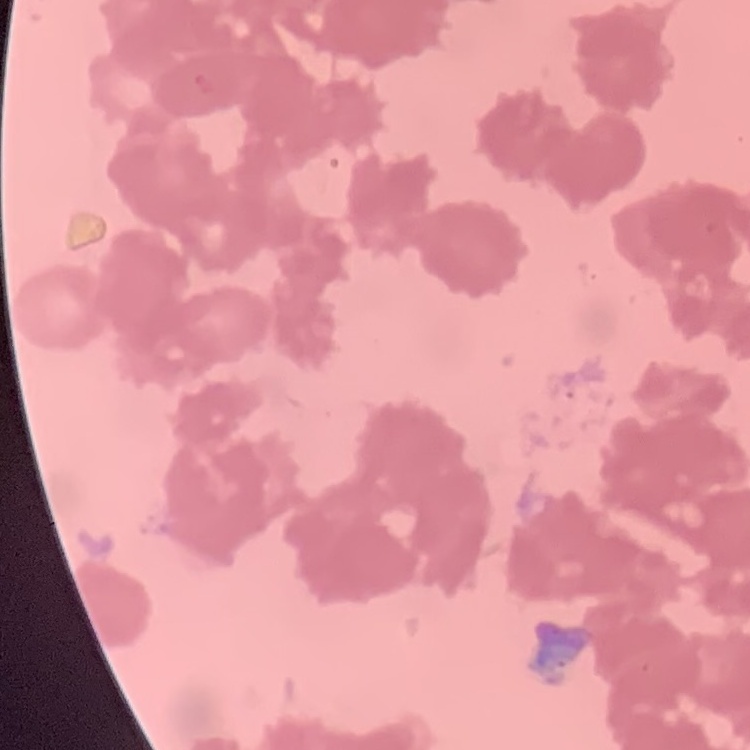

The erythrocytes exhibit rouleaux formation. Thin blood smear. Square crop of a larger photomicrograph. Stained with either Field's or Giemsa.